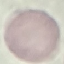

{
  "result": "no malaria parasites seen",
  "capture": "smartphone camera at the microscope eyepiece",
  "preparation": "thin blood smear",
  "image_type": "automatically extracted cell patch, resized to 64 × 64 pixels",
  "stain": "Giemsa"
}